Name the parasite shown.
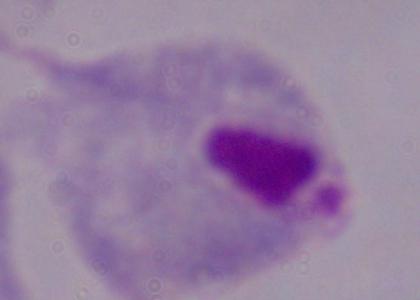

A trichomonad.

Summary:
  - Magnification: 1000x
  - Modality: photomicrograph